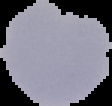

preparation: thin blood film
image_size: 112×106 pixels
malaria_status: uninfected
image_type: segmented cell region on a black background